State which parasite is depicted.
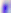

This is Toxoplasma gondii.

{
  "magnification": "400x",
  "modality": "photomicrograph"
}